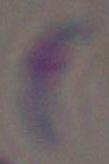

Summary:
  - Identification: Toxoplasma gondii
  - Modality: micrograph
  - Magnification: 1000x